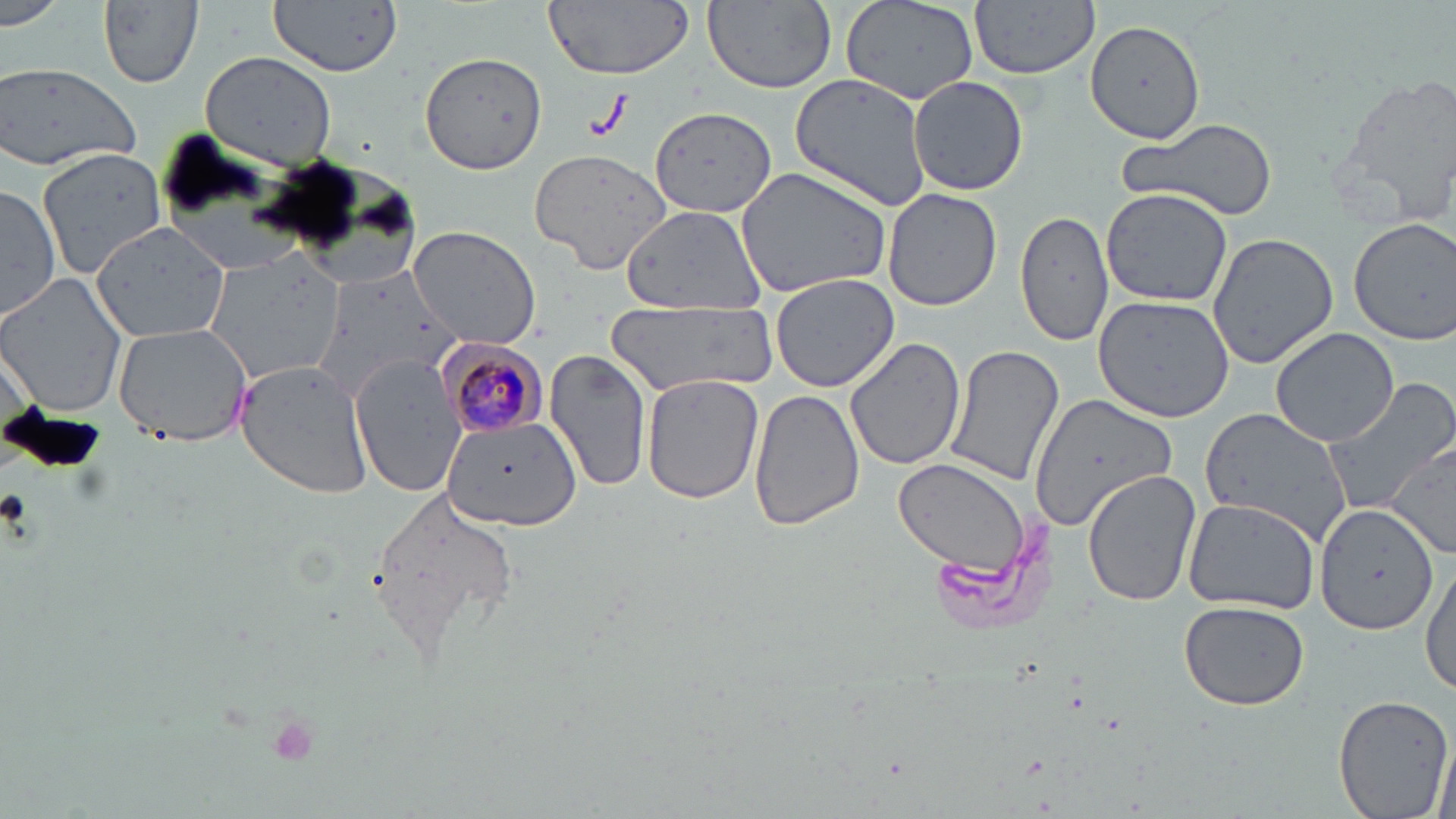
Approximate bounding boxes as (x1,y1)-(x2,y2) corner pairs in pixels. Plasmodium malariae-infected red blood cell locations: (435,337)-(550,439). Uninfected red blood cell locations: (0,0)-(65,29), (269,0)-(404,76), (543,0)-(695,80), (701,0)-(837,91), (841,0)-(976,104), (972,1)-(1101,78), (99,2)-(205,90), (1087,20)-(1204,143), (419,49)-(548,176), (199,50)-(336,170), (0,62)-(145,170), (1328,68)-(1456,227), (789,73)-(935,211), (908,76)-(1029,196), (651,107)-(776,217), (1118,116)-(1281,222), (532,146)-(672,275), (36,147)-(168,279), (734,167)-(894,297), (0,184)-(60,325), (882,189)-(1002,312), (1101,189)-(1233,307), (619,204)-(767,314), (1013,207)-(1115,346), (1349,216)-(1456,345), (88,224)-(232,343), (406,226)-(543,350), (1207,233)-(1338,370), (197,247)-(339,384), (314,263)-(460,406), (0,272)-(129,416), (769,272)-(899,392), (1092,296)-(1236,423), (608,303)-(772,396), (113,321)-(257,446), (1270,327)-(1398,446), (842,335)-(967,470), (946,345)-(1065,487), (545,348)-(654,493), (352,352)-(469,497), (235,359)-(377,499), (642,373)-(765,503), (1320,377)-(1456,514), (749,386)-(866,534), (1038,387)-(1185,565), (1197,405)-(1356,548), (442,418)-(584,531), (1387,443)-(1456,559), (892,458)-(1034,576), (1082,470)-(1202,608), (368,485)-(522,668), (1181,497)-(1321,613), (1315,503)-(1437,634), (1420,557)-(1456,702), (1178,600)-(1310,710), (1332,694)-(1453,819), (1432,722)-(1454,819). Slide-level diagnosis: Plasmodium malariae. One field of a larger specimen. 1000x magnification. Optical microscopy. Image is 1456×819 pixels. Thin blood film. May-Grünwald-Giemsa-stained preparation.